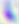

Micrograph. 400x magnification. Toxoplasma gondii is seen.